State which parasite is depicted.
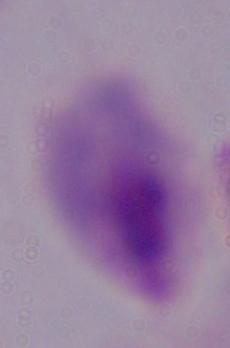

A trichomonad.

Captured at 1000x magnification. Micrograph.